State the blood parasite species.
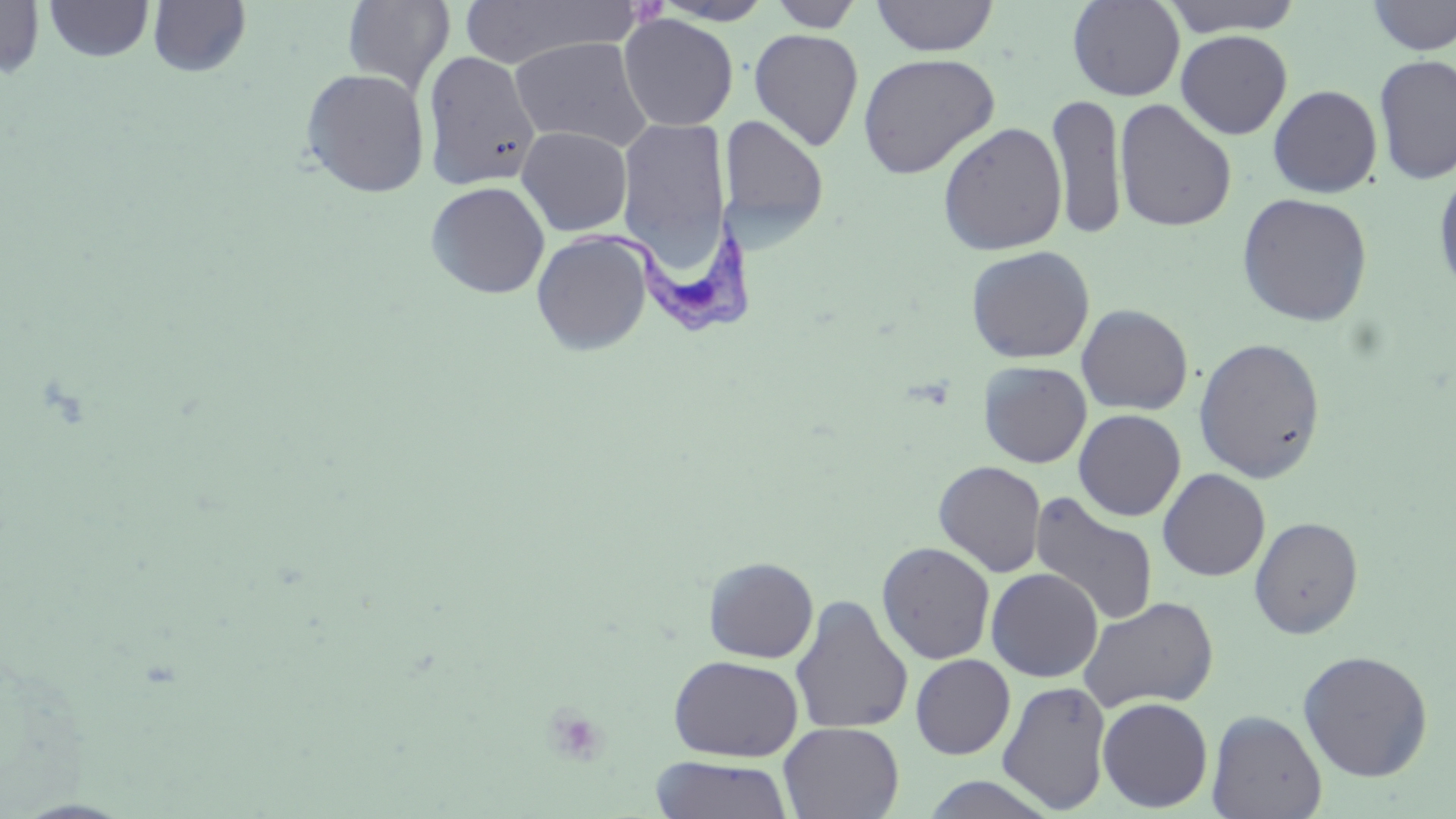
Trypanosoma brucei.

stain: May-Grünwald-Giemsa
image_size: 1456×819 pixels
preparation: thin blood smear
modality: optical microscopy
trypanosoma_brucei_locations: 'approximate bounding boxes as (x1,y1)-(x2,y2) corner pairs in pixels: (570,226)-(761,338)'
uninfected_red_blood_cell_locations: 'approximate bounding boxes as (x1,y1)-(x2,y2) corner pairs in pixels: (0,0)-(45,80), (147,0)-(252,77), (343,0)-(455,95), (768,0)-(865,32), (870,0)-(999,56), (1067,0)-(1185,101), (1159,0)-(1306,37), (1365,0)-(1456,55), (44,1)-(154,62), (457,1)-(638,68), (651,1)-(776,25), (618,13)-(738,131), (749,28)-(864,151), (1175,29)-(1293,140), (509,36)-(652,152), (422,51)-(542,190), (857,52)-(1000,179), (1374,54)-(1456,185), (299,68)-(430,198), (1268,85)-(1383,198), (1047,92)-(1127,240), (1114,99)-(1237,233), (719,114)-(829,245), (617,116)-(732,268), (938,122)-(1068,255), (516,125)-(633,236), (1433,167)-(1456,299), (425,181)-(550,299), (1237,192)-(1373,326), (531,230)-(653,357), (966,245)-(1095,364), (1076,304)-(1193,415), (1193,336)-(1327,483), (979,361)-(1091,468), (1074,409)-(1186,521), (934,460)-(1046,577), (1158,468)-(1271,581), (1030,492)-(1159,627), (1249,516)-(1364,639), (876,541)-(996,665), (703,556)-(819,663), (986,568)-(1103,682), (790,595)-(913,735), (1078,596)-(1219,713), (1297,649)-(1434,782), (668,654)-(804,762), (910,654)-(1015,759), (997,680)-(1112,814), (1097,697)-(1213,812), (1207,709)-(1327,819), (778,722)-(904,818), (651,756)-(794,818), (921,774)-(1058,818)'
magnification: 1000x
field_of_view: single